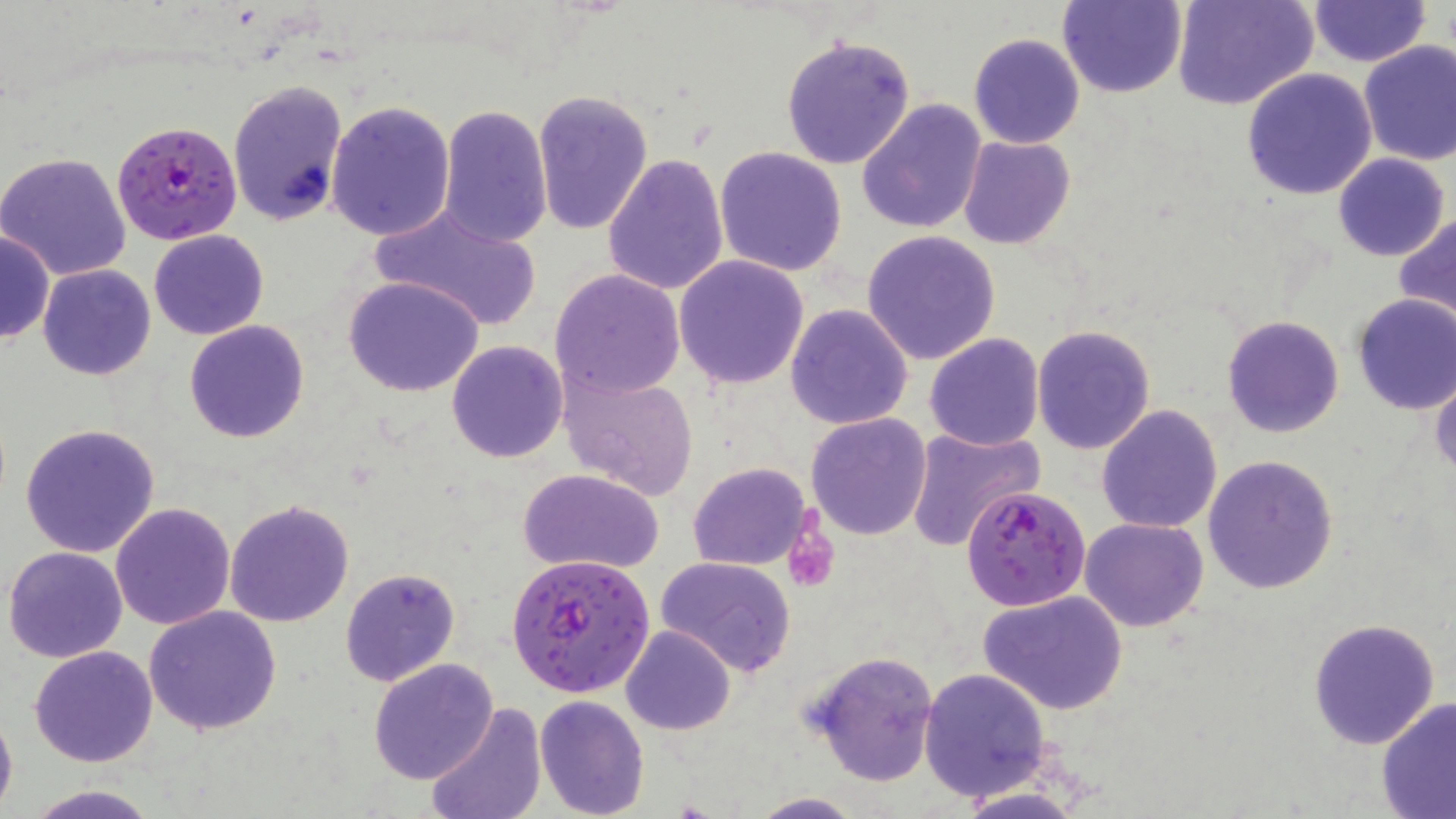 Approximate bounding boxes as (x1, y1, x2, y2) in pixels. Platelet locations: (784, 529, 838, 592). Plasmodium falciparum-infected red blood cell locations: (112, 119, 242, 246), (961, 485, 1091, 611), (505, 552, 655, 698). Uninfected red blood cell locations: (1056, 0, 1188, 98), (1174, 0, 1318, 111), (1308, 1, 1430, 67), (1200, 19, 1353, 161), (969, 32, 1085, 148), (779, 34, 916, 172), (1357, 40, 1456, 166), (1241, 69, 1378, 200), (226, 79, 348, 227), (531, 89, 654, 234), (857, 99, 989, 234), (325, 100, 456, 241), (437, 105, 553, 247), (957, 136, 1075, 250), (714, 146, 848, 277), (0, 151, 133, 281), (602, 153, 730, 294), (1332, 153, 1449, 261), (367, 200, 543, 331), (1395, 213, 1456, 325), (149, 229, 270, 340), (0, 230, 53, 344), (861, 230, 1001, 365), (675, 256, 810, 391), (38, 264, 156, 381), (549, 268, 686, 399), (343, 276, 485, 398), (1350, 293, 1456, 414), (786, 304, 914, 430), (1222, 314, 1345, 439), (184, 320, 310, 443), (1032, 324, 1157, 455), (924, 332, 1045, 451), (445, 339, 567, 463), (1428, 362, 1456, 479), (560, 370, 699, 500), (1097, 405, 1223, 534), (805, 412, 933, 541), (20, 422, 161, 558), (905, 426, 1045, 549), (1203, 454, 1339, 595), (685, 462, 814, 569), (517, 469, 667, 575), (224, 498, 354, 628), (111, 502, 234, 629), (1080, 516, 1209, 632), (4, 544, 129, 663), (656, 556, 800, 677), (339, 567, 461, 687), (979, 591, 1129, 716), (142, 605, 283, 736), (1307, 618, 1442, 751), (621, 625, 735, 735), (30, 645, 160, 767), (807, 649, 940, 788), (368, 659, 499, 784), (917, 665, 1052, 802), (534, 694, 649, 818), (1377, 697, 1456, 818), (0, 703, 17, 818), (425, 703, 546, 819), (23, 783, 163, 819), (746, 792, 866, 818). Slide-level diagnosis: Plasmodium falciparum. Thin blood film. Optical microscopy. 1000x magnification. Image is 1456×819 pixels. May-Grünwald-Giemsa-stained preparation. One field of a larger specimen.